Identify the blood parasite species.
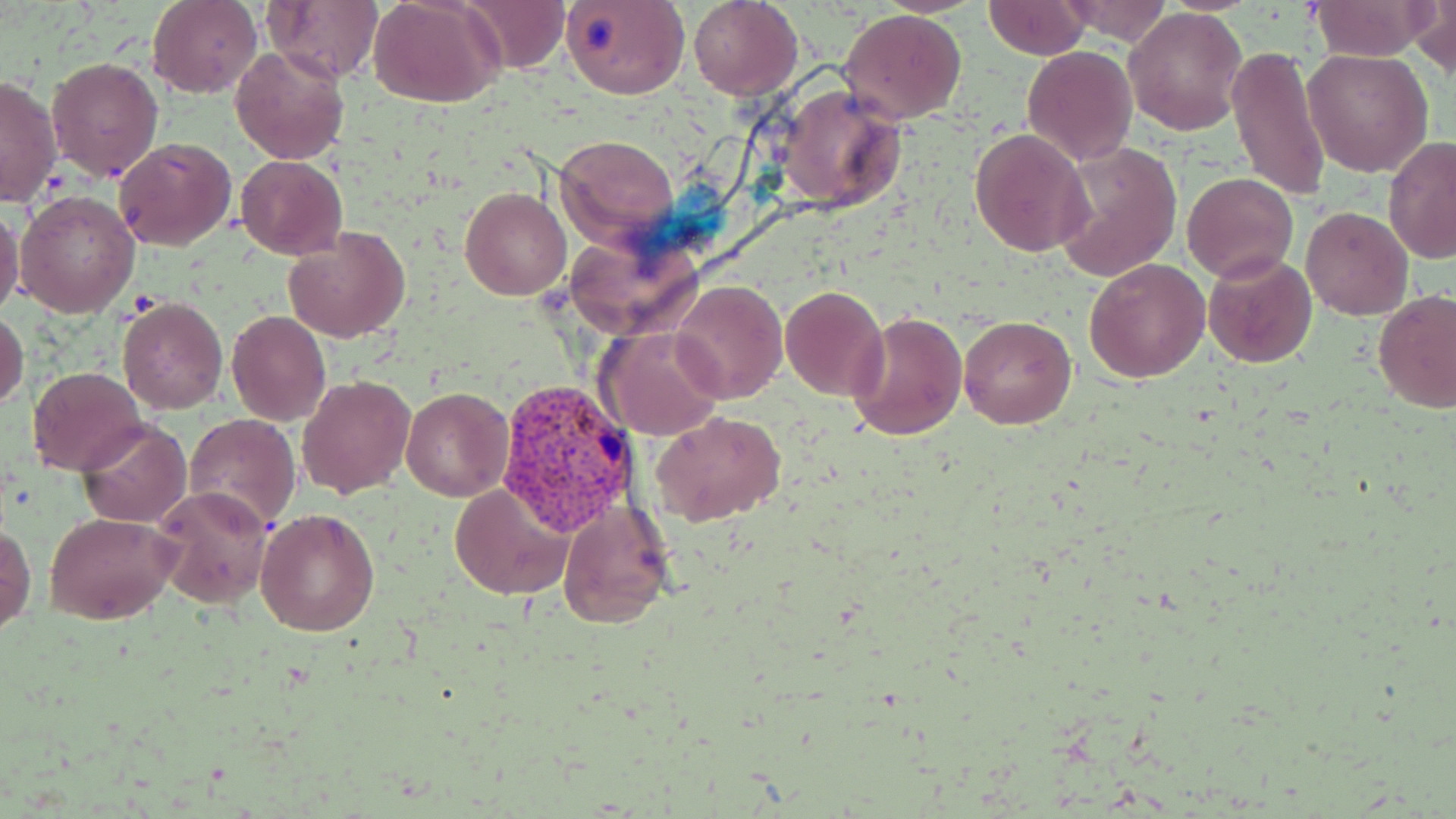

Plasmodium vivax.

field of view = single
magnification = 1000x
uninfected red blood cell locations = approximate bounding boxes as named x1/y1/x2/y2 corners in pixels: (x1=260, y1=0, x2=382, y2=83), (x1=371, y1=0, x2=504, y2=108), (x1=463, y1=0, x2=568, y2=74), (x1=564, y1=0, x2=688, y2=100), (x1=688, y1=0, x2=804, y2=99), (x1=1051, y1=0, x2=1173, y2=44), (x1=1308, y1=0, x2=1435, y2=62), (x1=148, y1=1, x2=261, y2=97), (x1=983, y1=1, x2=1090, y2=58), (x1=1412, y1=1, x2=1455, y2=78), (x1=1124, y1=6, x2=1248, y2=135), (x1=838, y1=9, x2=967, y2=124), (x1=1229, y1=44, x2=1331, y2=204), (x1=231, y1=45, x2=349, y2=165), (x1=1022, y1=45, x2=1137, y2=165), (x1=1304, y1=48, x2=1434, y2=177), (x1=45, y1=57, x2=164, y2=182), (x1=1, y1=74, x2=61, y2=211), (x1=776, y1=83, x2=905, y2=213), (x1=969, y1=127, x2=1093, y2=259), (x1=553, y1=134, x2=678, y2=246), (x1=1383, y1=136, x2=1455, y2=265), (x1=115, y1=138, x2=236, y2=251), (x1=1051, y1=141, x2=1182, y2=284), (x1=235, y1=154, x2=346, y2=259), (x1=1182, y1=172, x2=1297, y2=282), (x1=459, y1=187, x2=571, y2=300), (x1=15, y1=189, x2=139, y2=317), (x1=0, y1=201, x2=24, y2=322), (x1=1301, y1=205, x2=1413, y2=320), (x1=284, y1=226, x2=410, y2=343), (x1=565, y1=229, x2=703, y2=340), (x1=1203, y1=252, x2=1318, y2=368), (x1=1084, y1=258, x2=1211, y2=383), (x1=671, y1=280, x2=788, y2=403), (x1=779, y1=286, x2=889, y2=401), (x1=1374, y1=289, x2=1456, y2=414), (x1=117, y1=296, x2=228, y2=415), (x1=0, y1=309, x2=27, y2=409), (x1=845, y1=309, x2=967, y2=442), (x1=227, y1=311, x2=331, y2=427), (x1=958, y1=315, x2=1078, y2=429), (x1=598, y1=327, x2=726, y2=442), (x1=27, y1=366, x2=146, y2=476), (x1=297, y1=374, x2=415, y2=498), (x1=400, y1=388, x2=513, y2=501), (x1=651, y1=410, x2=787, y2=526), (x1=186, y1=413, x2=300, y2=532), (x1=76, y1=419, x2=190, y2=528), (x1=449, y1=482, x2=572, y2=599), (x1=151, y1=486, x2=271, y2=608), (x1=556, y1=501, x2=673, y2=629), (x1=255, y1=507, x2=381, y2=636), (x1=46, y1=511, x2=182, y2=625), (x1=1, y1=519, x2=35, y2=638)
Plasmodium vivax-infected red blood cell locations = approximate bounding boxes as named x1/y1/x2/y2 corners in pixels: (x1=494, y1=377, x2=639, y2=534)
image size = 1456×819 pixels
preparation = thin blood smear
stain = May-Grünwald-Giemsa
modality = optical microscopy